Locate every Plasmodium malariae-infected red blood cell.
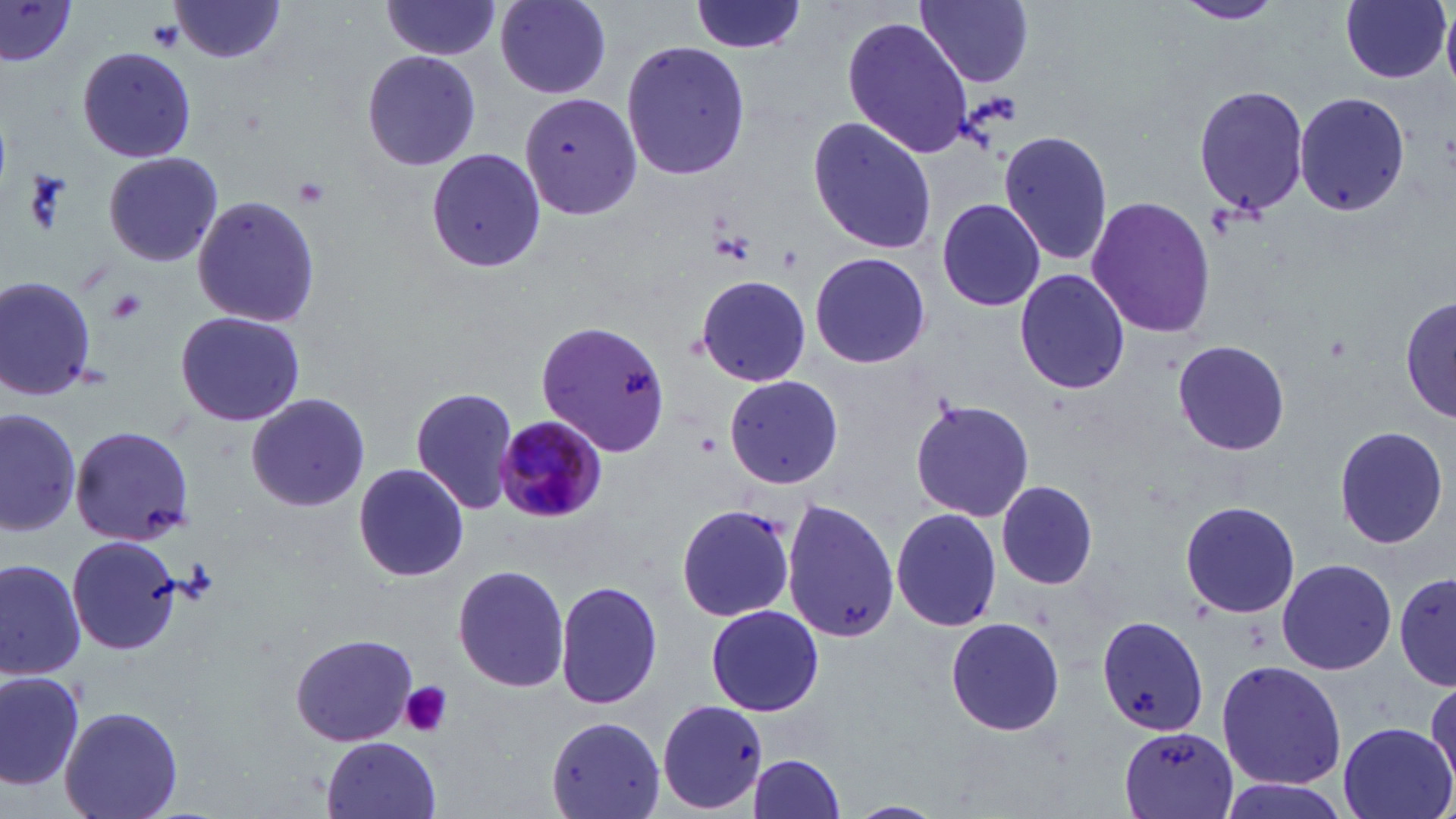

Approximate bounding boxes as [x1, y1, x2, y2] in pixels.
Plasmodium malariae-infected red blood cells: [493, 416, 606, 523].

slide-level diagnosis = Plasmodium malariae
stain = May-Grünwald-Giemsa
image size = 1456×819 pixels
platelet locations = approximate bounding boxes as [x1, y1, x2, y2] in pixels: [291, 177, 332, 211], [107, 289, 147, 323], [399, 681, 452, 738]
preparation = thin blood smear
uninfected red blood cell locations = approximate bounding boxes as [x1, y1, x2, y2] in pixels: [493, 0, 612, 99], [690, 0, 808, 56], [916, 0, 1035, 87], [1172, 0, 1285, 26], [1338, 0, 1451, 84], [0, 1, 80, 68], [167, 1, 290, 65], [378, 1, 502, 60], [1442, 10, 1456, 84], [841, 17, 973, 158], [620, 38, 752, 183], [76, 46, 197, 166], [359, 48, 483, 173], [1191, 82, 1309, 215], [1291, 91, 1410, 217], [517, 94, 644, 221], [805, 117, 938, 255], [998, 127, 1116, 267], [423, 147, 547, 276], [101, 151, 223, 269], [1084, 194, 1216, 341], [936, 196, 1045, 311], [190, 197, 323, 329], [807, 252, 932, 370], [1012, 268, 1132, 395], [0, 273, 104, 406], [693, 274, 810, 387], [1, 275, 101, 402], [696, 276, 813, 387], [1400, 291, 1453, 426], [175, 309, 306, 427], [533, 317, 675, 458], [1173, 339, 1290, 457], [724, 375, 843, 491], [410, 386, 517, 514], [246, 393, 370, 512], [911, 396, 1033, 523], [1, 406, 83, 538], [1334, 423, 1450, 550], [70, 426, 198, 548], [72, 426, 193, 546], [351, 462, 469, 582], [995, 479, 1098, 592], [1177, 498, 1302, 619], [782, 499, 900, 642], [674, 503, 798, 624], [890, 506, 1002, 635], [68, 536, 182, 655], [0, 555, 88, 680], [1276, 558, 1395, 677], [451, 563, 572, 695], [1393, 570, 1454, 691], [1395, 572, 1456, 688], [554, 579, 662, 713], [704, 604, 824, 716], [1095, 612, 1213, 738], [942, 615, 1067, 736], [289, 632, 418, 749], [1215, 661, 1347, 789], [0, 667, 84, 791], [1426, 676, 1456, 797], [655, 700, 772, 813], [60, 706, 185, 819], [545, 716, 664, 819], [546, 717, 669, 819], [1334, 721, 1454, 819], [1117, 726, 1241, 818], [320, 737, 444, 819], [745, 753, 846, 818], [1214, 776, 1354, 819], [844, 799, 950, 819]
field of view = single
magnification = 1000x
modality = light microscopy